Classify this cell by malaria status.
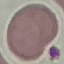
Uninfected.

image type = cell patch, automatically extracted from a larger field of view and resized to 64 × 64 pixels
stain = Giemsa
preparation = thin blood smear
capture = smartphone through the microscope eyepiece